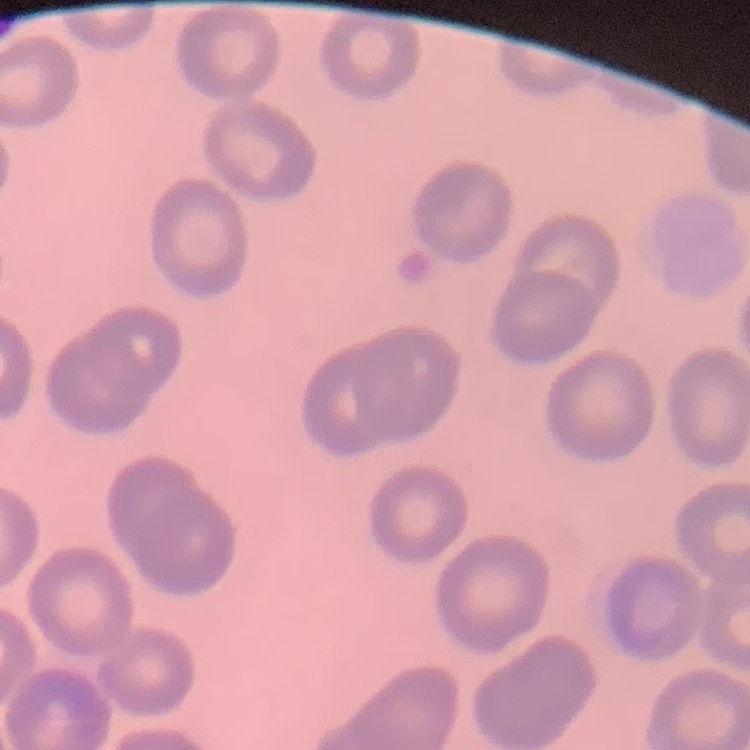

The red blood cells show no rouleaux formation. Thin blood smear. Stained with either Field's or Giemsa. Square crop of a larger photomicrograph.